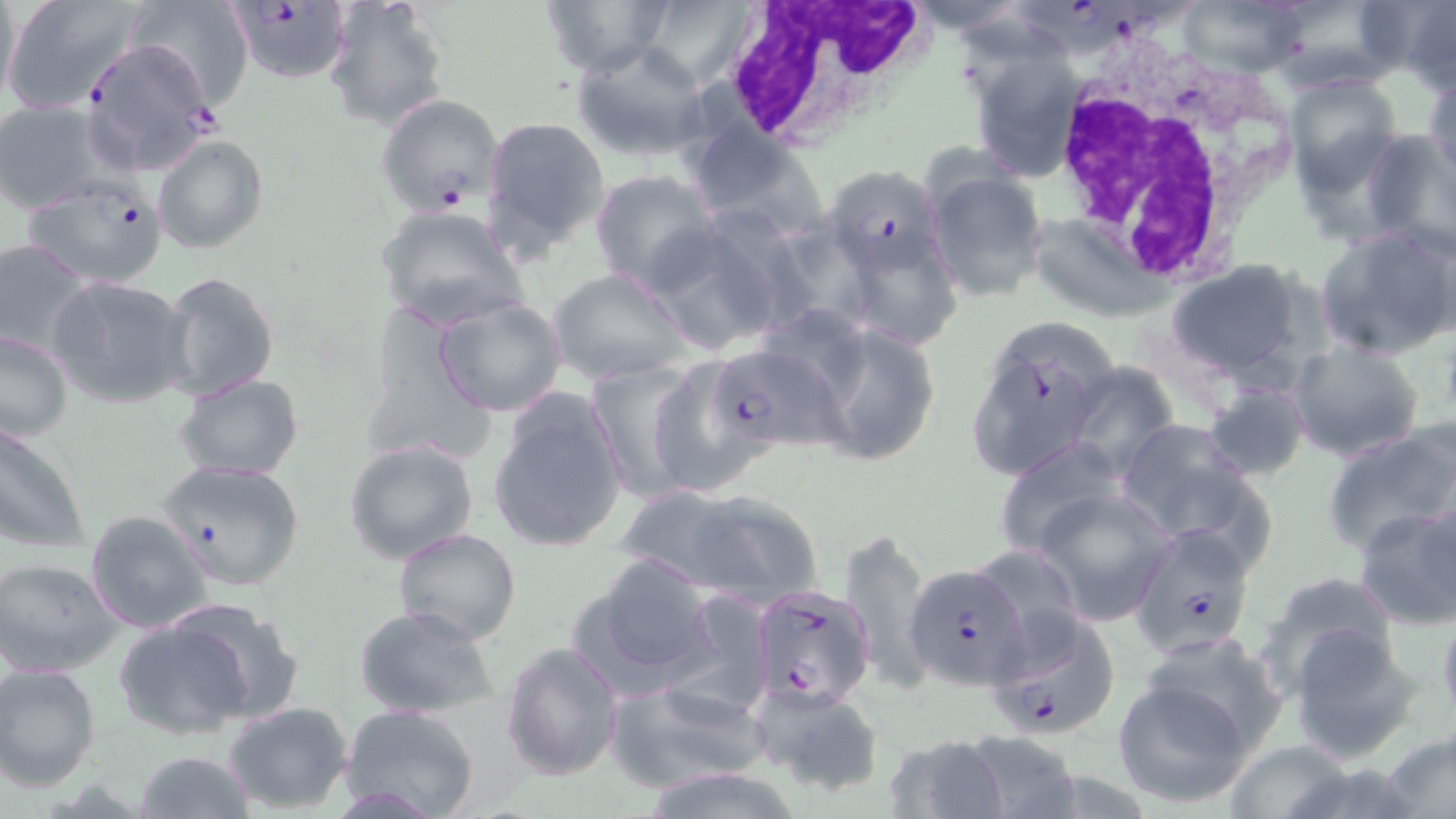

slide-level diagnosis = Plasmodium falciparum
magnification = 1000x
image size = 1456×819 pixels
white blood cell locations = approximate bounding boxes as (x1,y1)-(x2,y2) corner pairs in pixels: (718,0)-(931,150), (1045,41)-(1301,282)
field of view = single
modality = optical microscopy
preparation = thin blood film
Plasmodium falciparum-infected red blood cell locations = approximate bounding boxes as (x1,y1)-(x2,y2) corner pairs in pixels: (221,0)-(353,82), (1028,0)-(1181,59), (78,38)-(219,179), (375,93)-(503,215), (822,160)-(949,291), (22,176)-(171,288), (707,341)-(847,453), (157,459)-(305,591), (1128,520)-(1259,658), (905,561)-(1031,691), (747,584)-(874,710), (985,607)-(1119,748)
uninfected red blood cell locations = approximate bounding boxes as (x1,y1)-(x2,y2) corner pairs in pixels: (0,0)-(22,120), (2,0)-(146,117), (126,0)-(253,109), (324,0)-(449,131), (536,0)-(672,77), (904,0)-(1031,33), (1177,0)-(1312,80), (1350,0)-(1451,82), (638,1)-(754,85), (1402,2)-(1456,94), (572,41)-(710,162), (967,51)-(1087,181), (1425,68)-(1456,189), (1282,75)-(1402,192), (1,100)-(109,212), (482,116)-(609,256), (688,117)-(827,235), (1359,129)-(1456,260), (153,135)-(270,255), (923,164)-(1049,304), (588,168)-(719,293), (376,204)-(527,328), (776,208)-(870,327), (643,213)-(794,356), (1027,213)-(1167,320), (1315,226)-(1456,360), (0,237)-(98,360), (855,253)-(961,342), (1164,258)-(1324,391), (550,267)-(689,386), (158,270)-(280,401), (50,274)-(193,408), (432,296)-(570,419), (361,306)-(497,457), (802,320)-(943,468), (963,320)-(1117,486), (0,332)-(73,441), (1287,340)-(1426,463), (638,354)-(773,499), (585,359)-(706,504), (1060,366)-(1176,478), (174,374)-(305,482), (1203,382)-(1310,480), (487,389)-(628,554), (1111,419)-(1264,549), (1322,419)-(1456,559), (0,420)-(91,553), (993,438)-(1129,560), (344,439)-(479,565), (618,484)-(818,604), (1034,489)-(1173,624), (1351,498)-(1456,632), (85,510)-(214,633), (392,527)-(521,646), (840,527)-(933,697), (571,553)-(721,697), (0,557)-(124,677), (1253,572)-(1406,701), (164,600)-(308,724), (353,604)-(500,718), (1435,609)-(1456,733), (115,613)-(258,741), (1282,621)-(1429,761), (1137,631)-(1288,762), (501,641)-(625,780), (0,662)-(101,791), (606,676)-(768,794), (1111,676)-(1258,808), (747,683)-(884,798), (223,702)-(354,815), (341,703)-(481,819), (1380,729)-(1456,819), (956,731)-(1086,819), (881,732)-(1012,819), (133,750)-(254,818)
stain = May-Grünwald-Giemsa